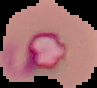

{
  "image_size": "97×88 pixels",
  "preparation": "thin blood smear",
  "result": "Plasmodium parasites identified",
  "image_type": "segmented cell region on a black background"
}